Report the malaria status of this cell.
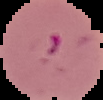
It is parasitized.

preparation = thin blood film
image size = 103×100 pixels
image type = segmented cell region on a black background